Locate every blood parasite and identify its species.
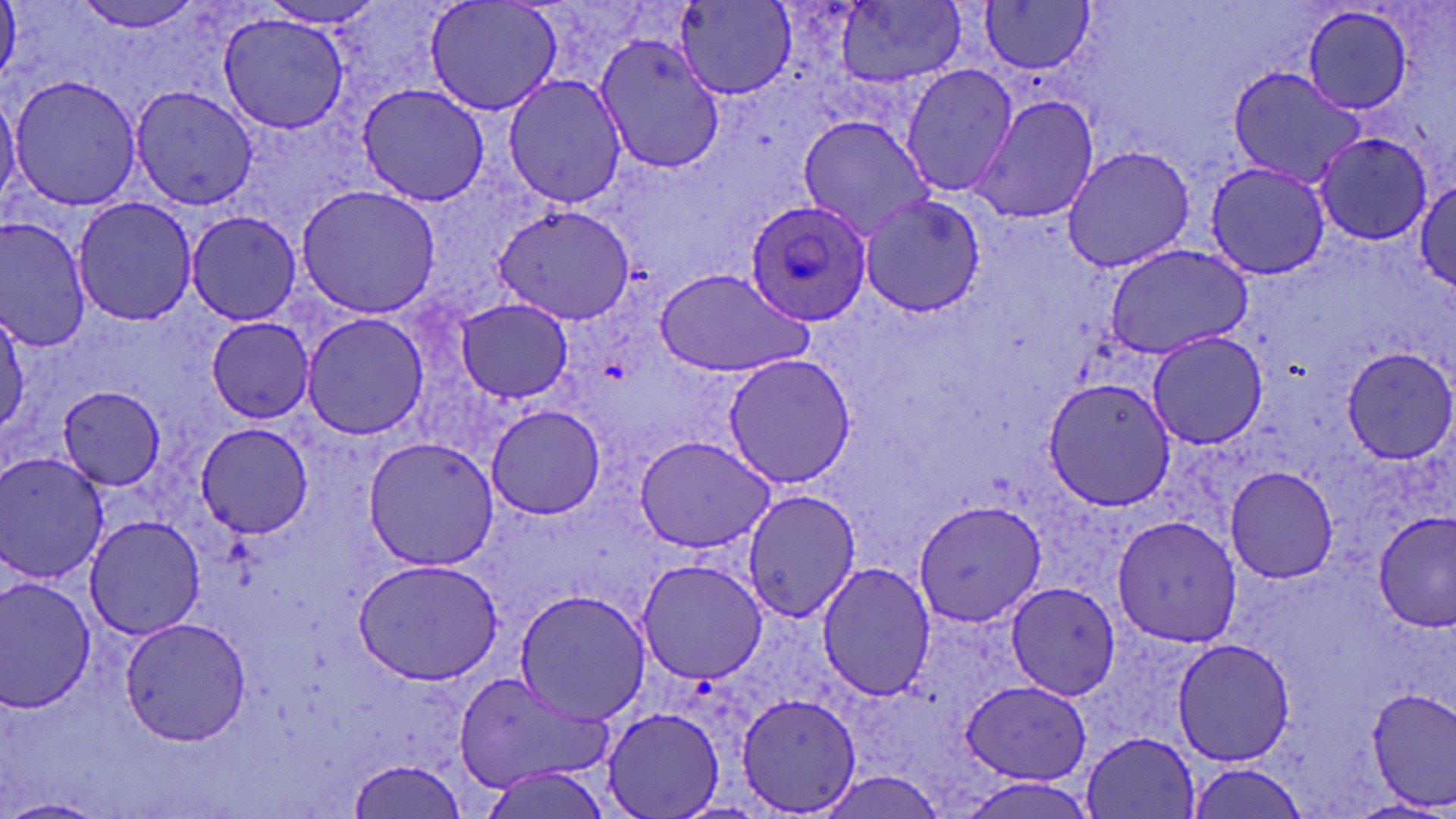

Approximate bounding boxes as [x1, y1, x2, y2] in pixels.
Plasmodium ovale-infected red blood cells: [744, 199, 875, 326].
No Plasmodium falciparum, Plasmodium malariae, Plasmodium vivax, Babesia divergens, or Trypanosoma brucei observed.

Uninfected red blood cell locations: [68, 0, 207, 35], [424, 0, 562, 120], [673, 0, 799, 99], [979, 2, 1097, 75], [834, 3, 967, 88], [1300, 6, 1417, 116], [217, 10, 355, 136], [594, 32, 730, 174], [900, 63, 1019, 198], [1227, 64, 1363, 185], [503, 73, 628, 208], [10, 76, 144, 211], [358, 83, 487, 208], [128, 84, 261, 211], [0, 85, 20, 206], [972, 93, 1100, 227], [798, 115, 933, 238], [1310, 131, 1432, 245], [1061, 143, 1196, 274], [1206, 162, 1332, 278], [1412, 175, 1456, 296], [296, 185, 442, 318], [861, 193, 988, 318], [71, 197, 196, 325], [493, 205, 635, 322], [186, 211, 300, 325], [0, 217, 91, 354], [1102, 244, 1252, 358], [653, 268, 815, 378], [454, 298, 576, 403], [1, 309, 27, 442], [301, 312, 430, 442], [203, 317, 315, 422], [1147, 331, 1270, 449], [1341, 346, 1455, 464], [720, 354, 855, 487], [1044, 378, 1175, 509], [58, 388, 167, 492], [486, 403, 606, 521], [193, 423, 314, 537], [633, 435, 775, 554], [364, 438, 499, 570], [1, 451, 109, 586], [1227, 466, 1340, 582], [740, 490, 864, 625], [912, 498, 1046, 628], [1376, 510, 1455, 630], [1110, 513, 1243, 648], [82, 514, 208, 641], [351, 558, 503, 684], [635, 558, 769, 683], [815, 561, 936, 701], [0, 575, 98, 713], [1006, 581, 1122, 701], [514, 589, 653, 724], [121, 616, 254, 744], [1172, 636, 1295, 766], [452, 671, 616, 793], [959, 680, 1091, 786], [1368, 689, 1456, 810], [734, 691, 861, 816], [602, 706, 723, 819], [1081, 731, 1203, 818], [349, 758, 470, 816], [1184, 761, 1314, 817], [818, 773, 950, 819], [1, 796, 108, 819]. Slide-level diagnosis: Plasmodium ovale. Optical microscopy. Image is 1456×819 pixels. May-Grünwald-Giemsa-stained preparation. 1000x magnification. One field of a larger specimen. Thin blood smear.